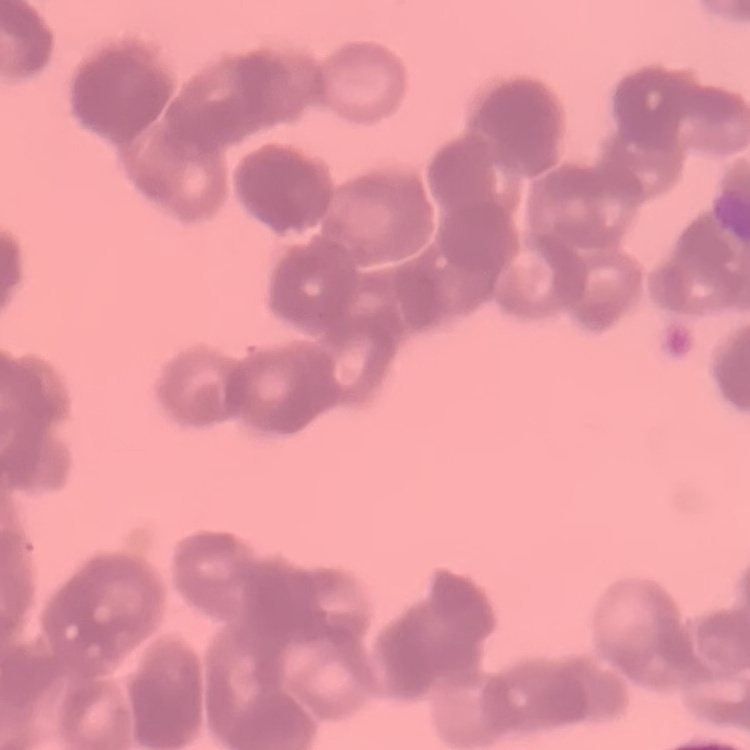

red blood cell morphology = rouleaux formation
image type = square crop of a larger photomicrograph
stain = Field's or Giemsa
preparation = thin blood smear